Name the cell type shown.
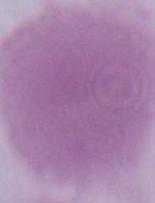

An erythrocyte.

1000x magnification. Micrograph.